Assess this cell for malaria.
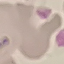
It is uninfected.

capture = smartphone through the microscope eyepiece
preparation = thin blood smear
stain = Giemsa
image type = automatically extracted cell patch, resized to 64 × 64 pixels